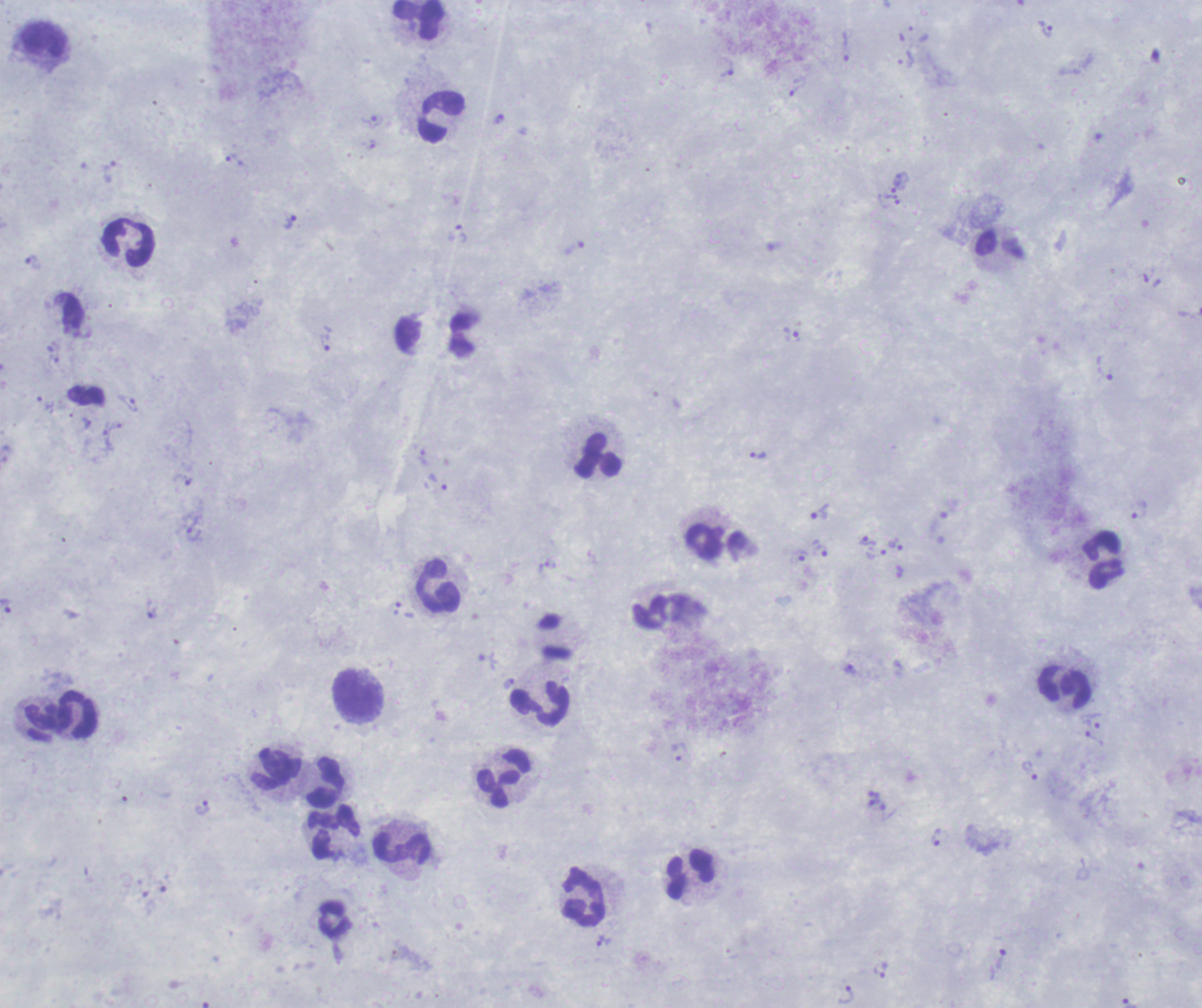
One field from this slide. Thick smear of blood. Romanowsky stain. Image is 1202×1008 pixels.